Classify this cell by malaria status.
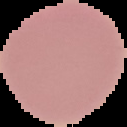
It is uninfected.

{
  "preparation": "thin blood smear",
  "image_type": "segmented cell region on a black background",
  "image_size": "127×127 pixels"
}